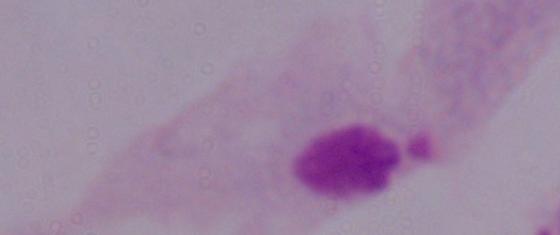

Summary:
  - Identification: trichomonad
  - Modality: micrograph
  - Magnification: 1000x